Classify this cell by malaria status.
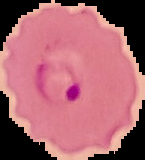

It is parasitized.

Summary:
  - Preparation: thin blood film
  - Image type: segmented cell region on a black background
  - Image size: 145×160 pixels